Locate and identify every blood parasite.
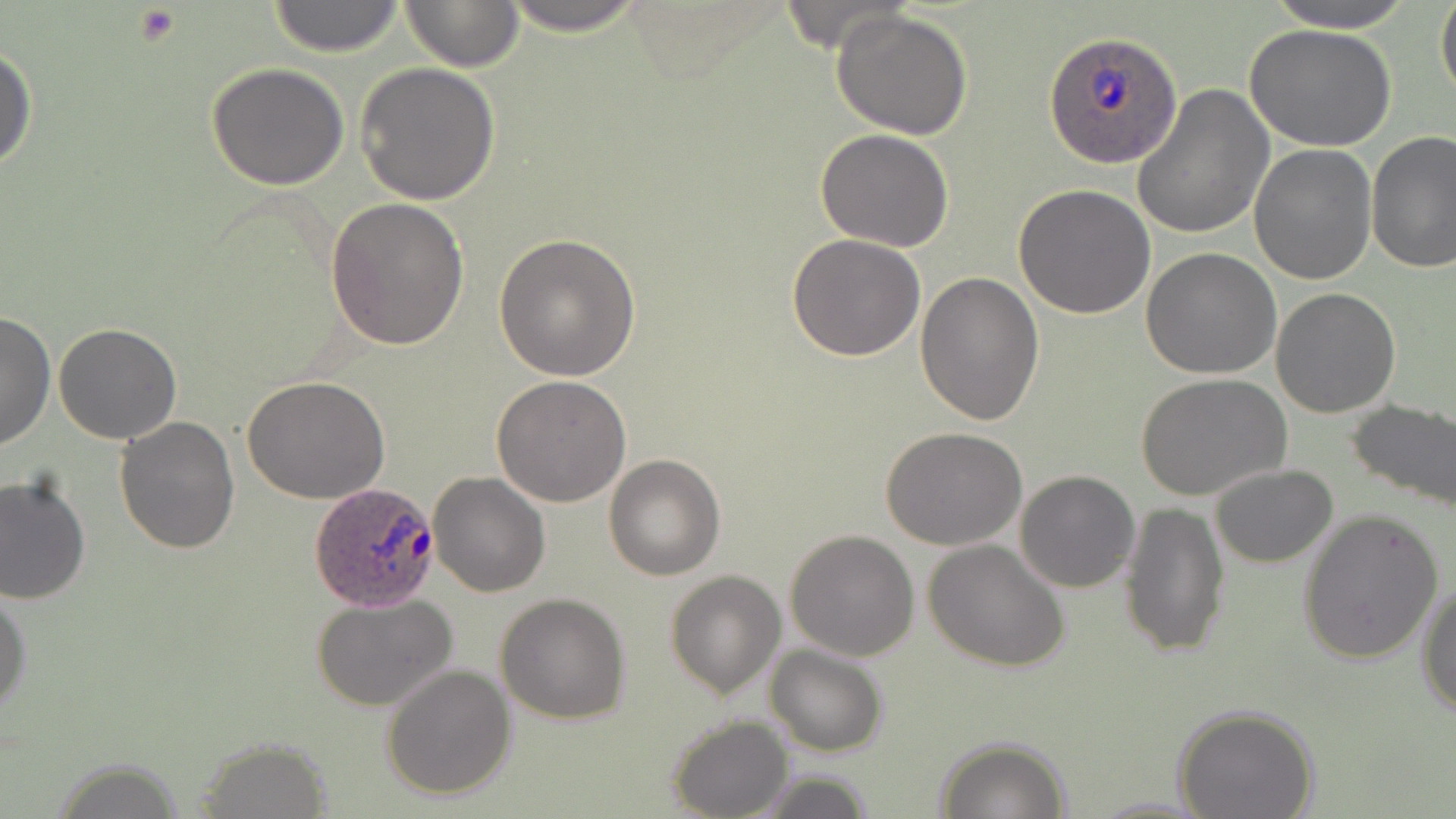
Approximate bounding boxes as (x1, y1, x2, y2) in pixels.
Plasmodium ovale-infected red blood cells: (1043, 32, 1183, 170), (309, 481, 441, 610).
No Plasmodium falciparum, Plasmodium malariae, Plasmodium vivax, Babesia divergens, or Trypanosoma brucei observed.

Platelet locations: (133, 5, 183, 45). Uninfected red blood cell locations: (265, 0, 407, 56), (398, 0, 526, 71), (490, 0, 656, 35), (1257, 0, 1422, 32), (1435, 0, 1456, 105), (830, 8, 974, 140), (1245, 23, 1396, 152), (0, 42, 37, 177), (355, 61, 500, 204), (205, 63, 351, 190), (1131, 84, 1274, 241), (814, 127, 955, 252), (1366, 131, 1456, 272), (1249, 145, 1378, 285), (1013, 185, 1156, 319), (327, 197, 468, 349), (495, 233, 641, 381), (785, 234, 925, 360), (1141, 248, 1282, 378), (913, 269, 1043, 425), (1270, 287, 1401, 418), (0, 310, 54, 452), (53, 323, 183, 444), (1136, 374, 1291, 504), (492, 375, 632, 506), (244, 377, 390, 503), (1344, 397, 1456, 514), (113, 417, 240, 555), (881, 426, 1028, 550), (603, 453, 727, 580), (1209, 464, 1337, 568), (1015, 470, 1141, 593), (428, 472, 550, 597), (0, 473, 91, 608), (1118, 500, 1230, 658), (1296, 508, 1444, 662), (785, 529, 920, 661), (923, 539, 1069, 672), (664, 569, 787, 698), (1417, 580, 1456, 717), (0, 587, 32, 719), (312, 593, 457, 714), (495, 593, 632, 724), (763, 644, 888, 757), (380, 663, 516, 800), (1172, 703, 1320, 819), (666, 715, 793, 819), (934, 736, 1070, 818), (191, 742, 334, 815), (48, 759, 193, 818), (747, 770, 877, 819), (1087, 796, 1216, 817). Slide-level diagnosis: Plasmodium ovale. Single field of view. Image is 1456×819 pixels. Optical microscopy. 1000x magnification. May-Grünwald-Giemsa stain. Thin blood smear.